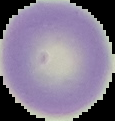

Summary:
  - Image type: segmented cell region on a black background
  - Image size: 115×121 pixels
  - Preparation: thin blood film
  - Malaria status: uninfected